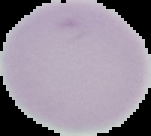
Summary:
  - Image size: 151×136 pixels
  - Image type: segmented cell region on a black background
  - Preparation: thin blood film
  - Result: negative for Plasmodium parasites